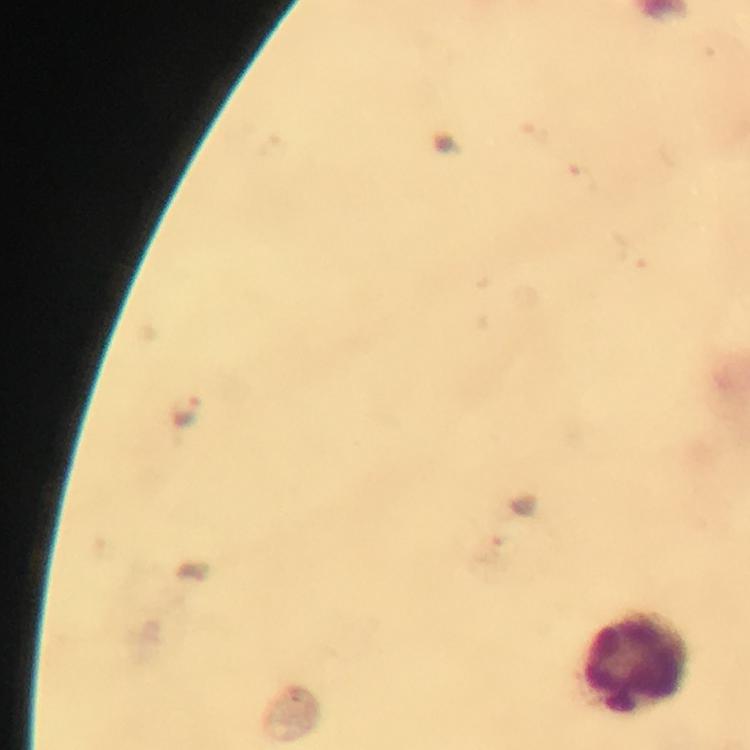

Approximate centers as {x, y} in pixels.
Summary:
  - Leukocyte locations: {637, 664}
  - Malaria parasite locations: {184, 413}
  - Capture: smartphone camera through the microscope
  - Context: from a malaria diagnostic workup
  - Stain: Giemsa
  - Image size: 750×750 pixels
  - Cropped from: a single field of view
  - Immersion oil: applied
  - Preparation: thick blood smear
  - Magnification: 100x